Assess this cell for malaria.
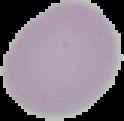
Uninfected.

Summary:
  - Image size: 124×121 pixels
  - Preparation: thin blood smear
  - Image type: cell region segmented out of the field of view; surrounding area masked to black